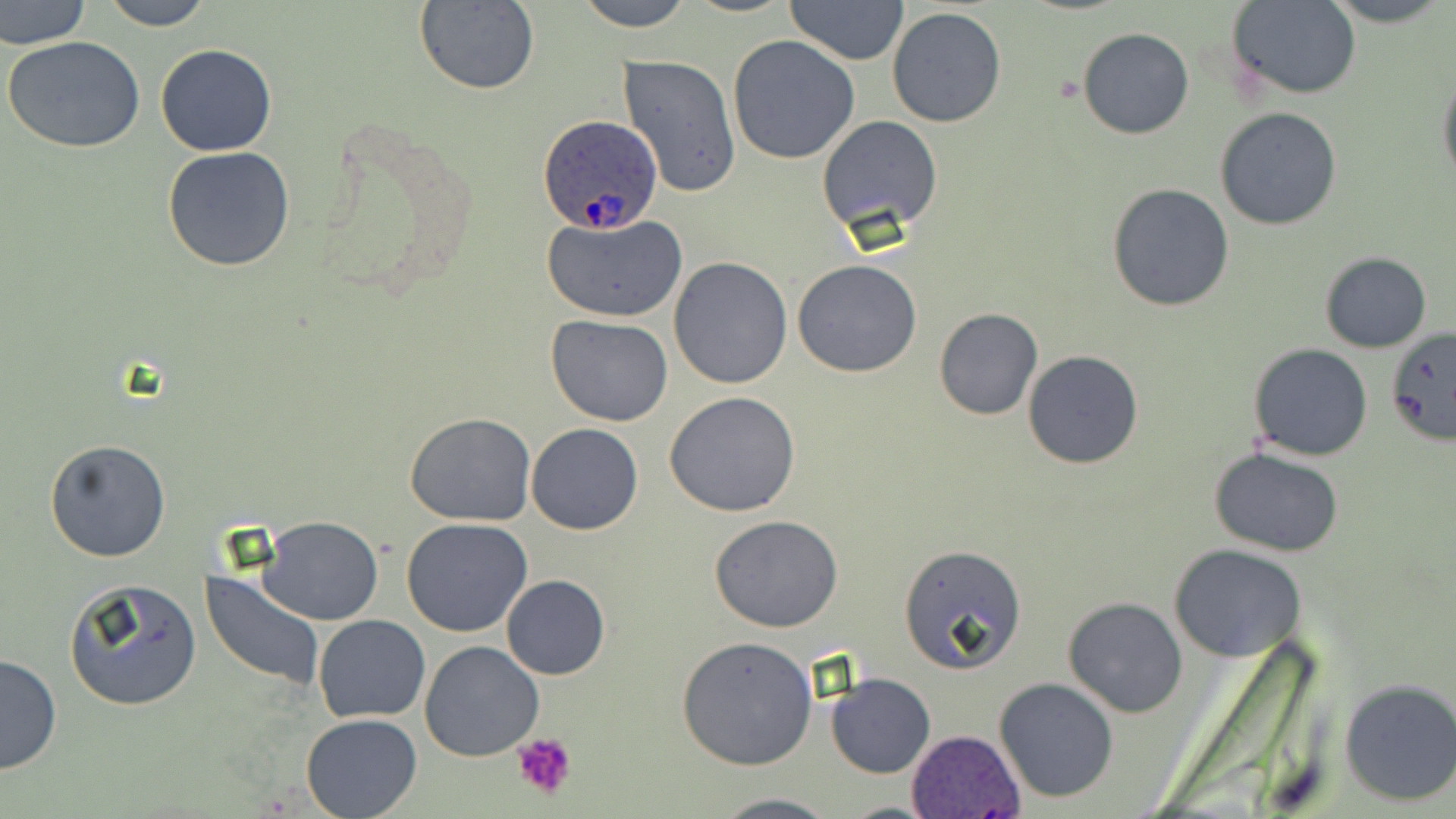
Approximate bounding boxes as (x1, y1, x2, y2) in pixels. Platelet locations: (512, 732, 577, 802). Plasmodium ovale-infected red blood cell locations: (535, 117, 663, 235), (905, 730, 1026, 817). Uninfected red blood cell locations: (0, 0, 90, 51), (96, 0, 214, 30), (572, 0, 696, 30), (785, 0, 910, 67), (1323, 0, 1449, 27), (413, 1, 540, 95), (1229, 1, 1360, 99), (887, 6, 1007, 128), (1078, 28, 1194, 140), (3, 35, 145, 153), (728, 35, 860, 164), (155, 43, 277, 158), (618, 55, 742, 196), (1437, 67, 1456, 192), (1214, 107, 1343, 231), (816, 115, 945, 240), (163, 146, 296, 271), (1107, 183, 1235, 312), (540, 212, 688, 323), (1319, 252, 1432, 353), (668, 257, 794, 389), (792, 259, 922, 378), (934, 308, 1042, 421), (546, 315, 673, 425), (1384, 326, 1456, 448), (1248, 344, 1373, 461), (1022, 350, 1144, 470), (663, 390, 804, 517), (405, 412, 536, 526), (525, 423, 644, 535), (44, 439, 172, 563), (1210, 446, 1344, 557), (709, 515, 843, 632), (259, 516, 383, 624), (401, 518, 534, 637), (898, 544, 1028, 674), (1169, 546, 1308, 662), (202, 573, 326, 691), (500, 574, 610, 680), (65, 578, 202, 712), (1062, 598, 1188, 718), (314, 615, 431, 722), (677, 635, 818, 770), (420, 640, 543, 761), (0, 652, 61, 776), (826, 673, 936, 778), (994, 677, 1121, 803), (1338, 677, 1456, 806), (299, 714, 421, 819), (708, 793, 841, 819). Slide-level diagnosis: Plasmodium ovale. May-Grünwald-Giemsa-stained preparation. Optical microscopy. Single field of view. Captured at 1000x magnification. Image is 1456×819 pixels. Thin blood smear.